Classify this cell by malaria status.
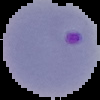

Parasitized.

From a thin blood smear. Image is 100×100 pixels. Segmented cell region on a black background.